Classify this cell by malaria status.
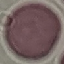
Uninfected.

Summary:
  - Preparation: thin blood smear
  - Capture: smartphone camera at the microscope eyepiece
  - Stain: Giemsa
  - Image type: automatically extracted cell patch, resized to 64 × 64 pixels